Assess the morphology of the erythrocytes.
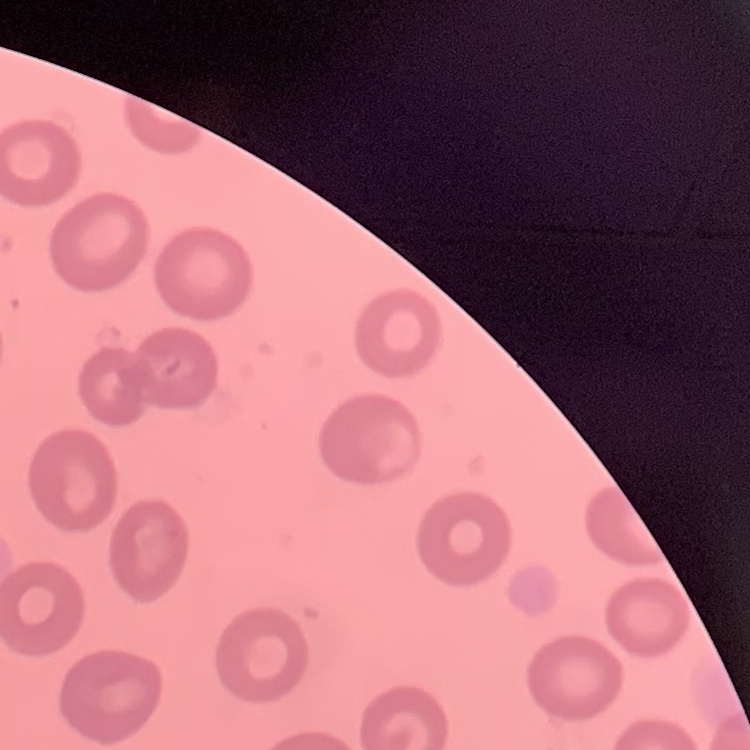

They show no rouleaux formation.

image_type: square crop of a larger photomicrograph
preparation: thin blood smear
stain: Field's or Giemsa